Name the blood parasite species.
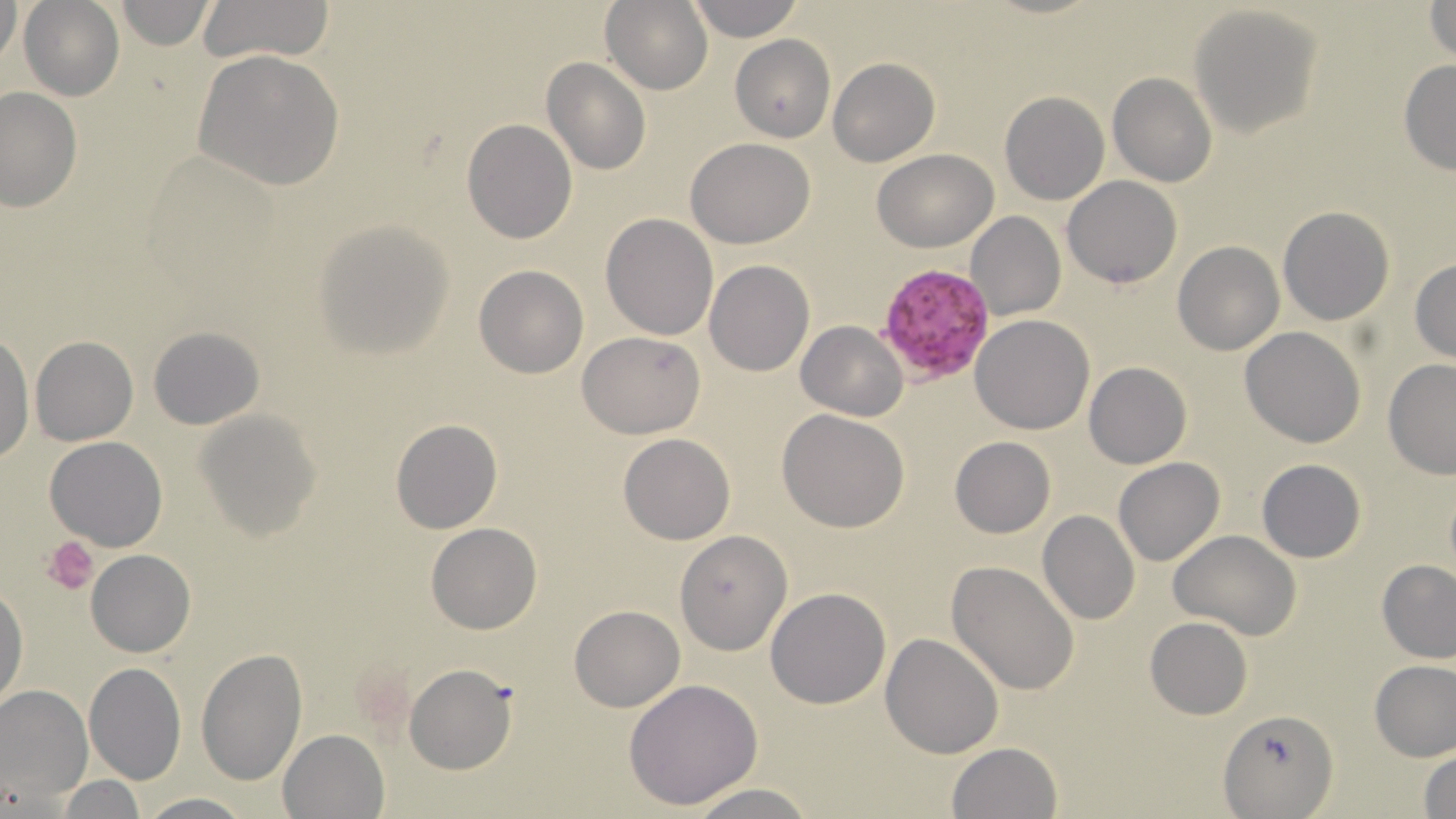
Plasmodium falciparum.

Approximate bounding boxes as named x1/y1/x2/y2 corners in pixels. Plasmodium falciparum-infected red blood cell locations: (x1=877, y1=262, x2=999, y2=385). Uninfected red blood cell locations: (x1=2, y1=0, x2=25, y2=75), (x1=19, y1=0, x2=124, y2=101), (x1=196, y1=0, x2=337, y2=65), (x1=686, y1=0, x2=803, y2=41), (x1=112, y1=1, x2=215, y2=49), (x1=601, y1=1, x2=712, y2=95), (x1=1426, y1=1, x2=1455, y2=64), (x1=1190, y1=4, x2=1322, y2=138), (x1=730, y1=34, x2=836, y2=142), (x1=734, y1=46, x2=941, y2=152), (x1=193, y1=50, x2=344, y2=191), (x1=828, y1=57, x2=939, y2=166), (x1=1398, y1=58, x2=1456, y2=177), (x1=542, y1=59, x2=650, y2=175), (x1=1108, y1=73, x2=1217, y2=187), (x1=1, y1=86, x2=81, y2=210), (x1=999, y1=93, x2=1109, y2=206), (x1=462, y1=119, x2=577, y2=244), (x1=686, y1=138, x2=815, y2=249), (x1=873, y1=148, x2=999, y2=252), (x1=1063, y1=176, x2=1183, y2=288), (x1=1279, y1=206, x2=1394, y2=326), (x1=601, y1=212, x2=718, y2=339), (x1=966, y1=212, x2=1065, y2=321), (x1=314, y1=220, x2=454, y2=357), (x1=1172, y1=240, x2=1284, y2=356), (x1=1410, y1=257, x2=1456, y2=364), (x1=704, y1=259, x2=814, y2=377), (x1=474, y1=265, x2=588, y2=378), (x1=970, y1=314, x2=1095, y2=434), (x1=796, y1=320, x2=907, y2=419), (x1=148, y1=326, x2=264, y2=430), (x1=1240, y1=326, x2=1365, y2=447), (x1=0, y1=330, x2=34, y2=462), (x1=578, y1=331, x2=705, y2=438), (x1=30, y1=336, x2=139, y2=445), (x1=1383, y1=360, x2=1456, y2=479), (x1=1084, y1=362, x2=1192, y2=469), (x1=196, y1=407, x2=323, y2=539), (x1=777, y1=410, x2=910, y2=532), (x1=392, y1=419, x2=501, y2=533), (x1=618, y1=433, x2=736, y2=545), (x1=44, y1=437, x2=168, y2=552), (x1=950, y1=437, x2=1055, y2=537), (x1=1114, y1=458, x2=1224, y2=567), (x1=1257, y1=459, x2=1366, y2=563), (x1=1037, y1=510, x2=1140, y2=625), (x1=427, y1=523, x2=542, y2=632), (x1=674, y1=529, x2=794, y2=656), (x1=1168, y1=530, x2=1300, y2=639), (x1=86, y1=549, x2=196, y2=658), (x1=1377, y1=559, x2=1456, y2=663), (x1=946, y1=560, x2=1080, y2=697), (x1=1, y1=584, x2=27, y2=709), (x1=767, y1=587, x2=891, y2=708), (x1=571, y1=605, x2=684, y2=711), (x1=1144, y1=616, x2=1253, y2=720), (x1=880, y1=632, x2=1003, y2=759), (x1=195, y1=647, x2=308, y2=786), (x1=1370, y1=658, x2=1456, y2=761), (x1=83, y1=663, x2=186, y2=785), (x1=404, y1=664, x2=516, y2=774), (x1=623, y1=678, x2=766, y2=811), (x1=0, y1=684, x2=93, y2=805), (x1=1219, y1=705, x2=1337, y2=817), (x1=278, y1=728, x2=389, y2=819), (x1=946, y1=742, x2=1062, y2=819), (x1=1417, y1=748, x2=1456, y2=817), (x1=53, y1=775, x2=150, y2=817), (x1=682, y1=783, x2=820, y2=819), (x1=136, y1=793, x2=255, y2=818). Platelet locations: (x1=45, y1=536, x2=100, y2=597). Light microscopy. May-Grünwald-Giemsa stain. Thin blood film. Image is 1456×819 pixels. Single field of view. Captured at 1000x magnification.